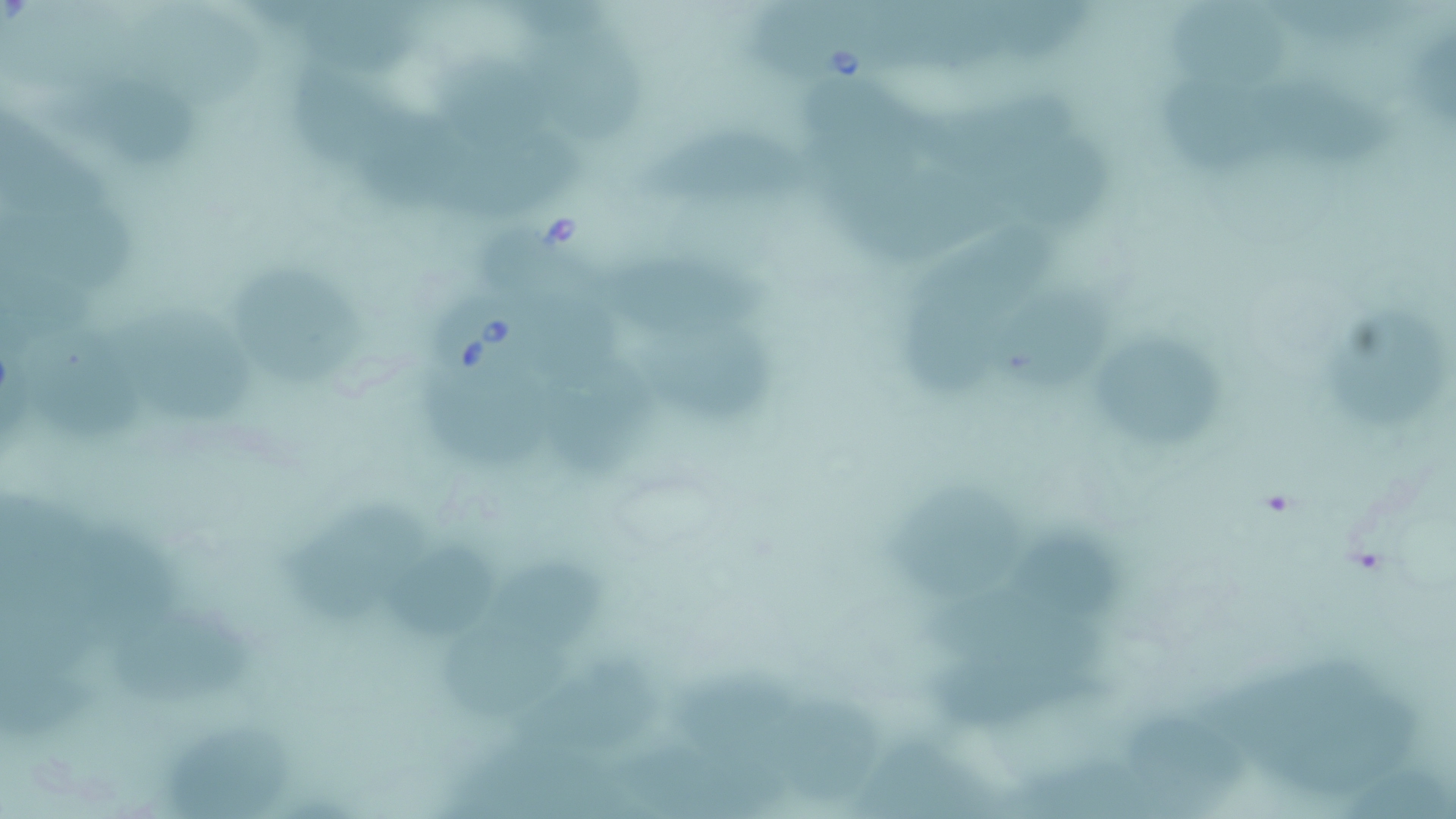
Approximate bounding boxes as named x1/y1/x2/y2 corners in pixels. Babesia divergens-infected red blood cell locations: (x1=757, y1=0, x2=881, y2=92), (x1=421, y1=285, x2=542, y2=400). Uninfected red blood cell locations: (x1=885, y1=0, x2=1019, y2=82), (x1=1009, y1=0, x2=1103, y2=65), (x1=307, y1=2, x2=428, y2=82), (x1=1263, y1=2, x2=1425, y2=52), (x1=1169, y1=5, x2=1300, y2=89), (x1=509, y1=17, x2=656, y2=147), (x1=449, y1=57, x2=568, y2=145), (x1=298, y1=68, x2=416, y2=166), (x1=70, y1=76, x2=205, y2=172), (x1=1160, y1=76, x2=1295, y2=179), (x1=1274, y1=81, x2=1397, y2=174), (x1=815, y1=89, x2=944, y2=188), (x1=918, y1=93, x2=1078, y2=167), (x1=0, y1=105, x2=133, y2=219), (x1=362, y1=109, x2=480, y2=215), (x1=646, y1=125, x2=814, y2=210), (x1=446, y1=127, x2=594, y2=225), (x1=1030, y1=148, x2=1115, y2=229), (x1=831, y1=166, x2=1022, y2=254), (x1=11, y1=200, x2=146, y2=292), (x1=930, y1=222, x2=1077, y2=310), (x1=493, y1=224, x2=626, y2=321), (x1=599, y1=249, x2=792, y2=347), (x1=237, y1=267, x2=371, y2=387), (x1=1000, y1=281, x2=1107, y2=389), (x1=906, y1=283, x2=1011, y2=395), (x1=115, y1=299, x2=259, y2=426), (x1=1337, y1=310, x2=1444, y2=435), (x1=33, y1=324, x2=154, y2=454), (x1=647, y1=330, x2=791, y2=432), (x1=1098, y1=334, x2=1231, y2=444), (x1=554, y1=356, x2=660, y2=475), (x1=444, y1=389, x2=567, y2=487), (x1=889, y1=479, x2=1036, y2=596), (x1=292, y1=491, x2=429, y2=623), (x1=1020, y1=522, x2=1129, y2=612), (x1=84, y1=529, x2=190, y2=636), (x1=393, y1=538, x2=511, y2=640), (x1=503, y1=550, x2=625, y2=637), (x1=5, y1=568, x2=118, y2=684), (x1=916, y1=584, x2=1101, y2=674), (x1=119, y1=608, x2=260, y2=704), (x1=440, y1=615, x2=589, y2=717), (x1=4, y1=647, x2=107, y2=749), (x1=515, y1=647, x2=662, y2=746), (x1=937, y1=648, x2=1114, y2=733), (x1=1215, y1=650, x2=1393, y2=743), (x1=678, y1=662, x2=818, y2=754), (x1=1259, y1=686, x2=1429, y2=784), (x1=786, y1=695, x2=892, y2=794), (x1=1122, y1=695, x2=1239, y2=806), (x1=164, y1=718, x2=290, y2=818), (x1=602, y1=734, x2=800, y2=819), (x1=858, y1=734, x2=1004, y2=819), (x1=1014, y1=743, x2=1185, y2=819), (x1=1345, y1=758, x2=1456, y2=819). Slide-level diagnosis: Babesia divergens. Light microscopy. Single field of view. 1000x magnification. Thin blood film. Image is 1456×819 pixels. May-Grünwald-Giemsa stain.